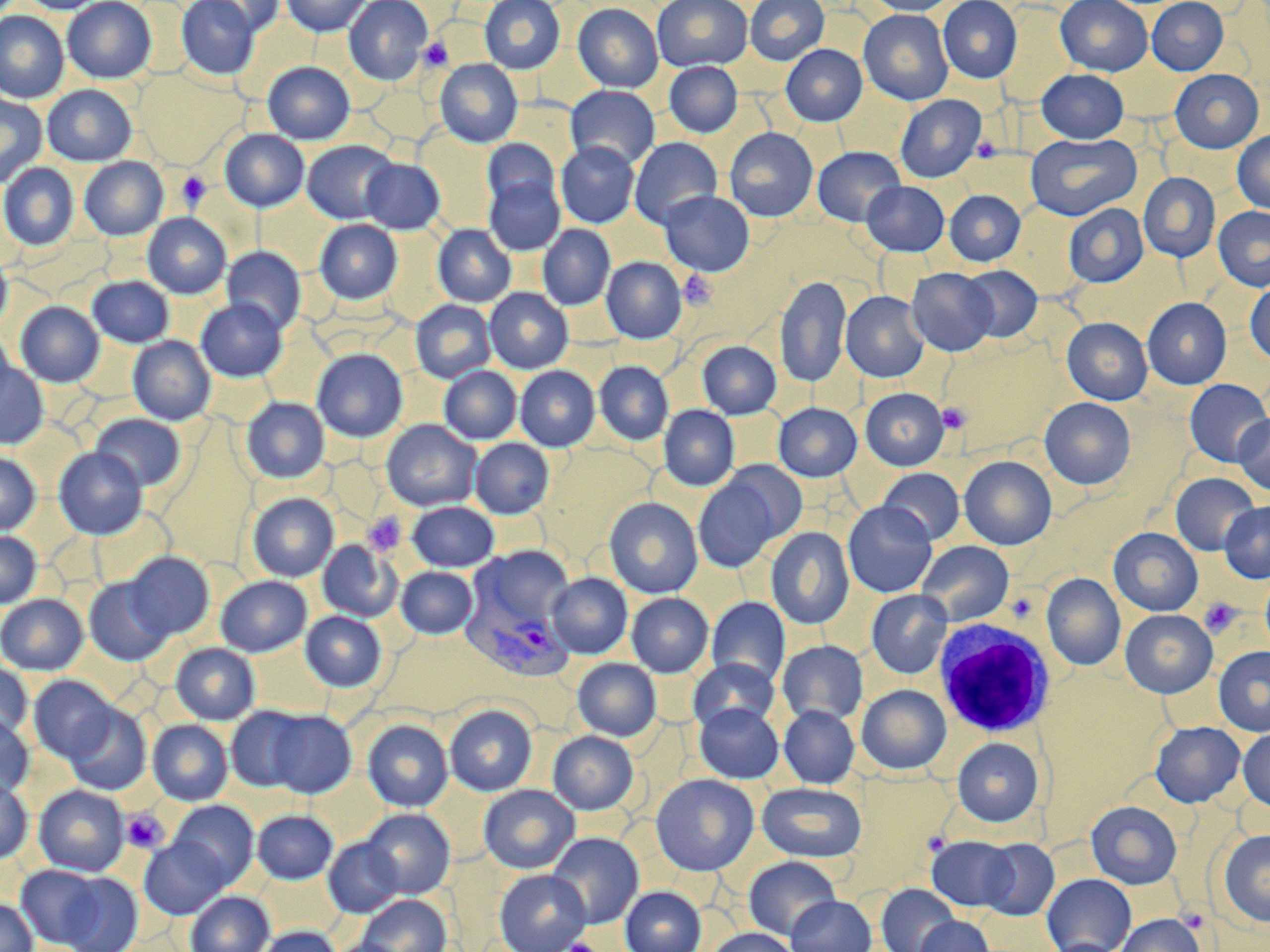

Approximate bounding boxes as [x1, y1, x2, y2] in pixels. Plasmodium vivax-infected red blood cell locations: [462, 591, 574, 681]. White blood cell locations: [932, 617, 1057, 737]. Uninfected red blood cell locations: [19, 0, 106, 14], [62, 0, 156, 83], [176, 0, 260, 80], [200, 0, 283, 36], [281, 0, 369, 36], [344, 0, 432, 85], [480, 0, 565, 74], [652, 0, 753, 72], [745, 0, 829, 65], [865, 0, 959, 15], [1055, 0, 1153, 75], [1147, 0, 1228, 75], [938, 1, 1022, 83], [572, 3, 663, 92], [859, 9, 953, 105], [0, 11, 68, 103], [781, 44, 867, 126], [435, 59, 522, 147], [262, 61, 354, 144], [664, 62, 743, 137], [133, 69, 244, 168], [1036, 69, 1129, 143], [1170, 69, 1264, 153], [42, 85, 137, 166], [565, 85, 660, 169], [0, 92, 47, 189], [895, 94, 986, 183], [724, 127, 818, 221], [219, 129, 309, 212], [1233, 130, 1270, 213], [1026, 134, 1141, 220], [630, 137, 723, 228], [483, 139, 560, 212], [302, 140, 399, 224], [556, 141, 639, 228], [812, 146, 906, 226], [79, 157, 168, 240], [361, 158, 445, 233], [0, 163, 79, 250], [1138, 173, 1220, 262], [484, 175, 565, 256], [862, 181, 949, 256], [944, 189, 1026, 266], [659, 190, 754, 276], [1063, 204, 1148, 287], [1214, 206, 1270, 291], [143, 213, 231, 298], [315, 220, 402, 304], [432, 224, 516, 307], [538, 224, 615, 310], [222, 246, 306, 334], [0, 248, 12, 332], [602, 257, 686, 343], [960, 265, 1043, 342], [907, 267, 998, 356], [775, 275, 851, 388], [88, 276, 174, 347], [1245, 280, 1270, 364], [485, 288, 573, 373], [841, 291, 928, 382], [1142, 297, 1231, 389], [196, 299, 287, 382], [411, 300, 496, 383], [15, 301, 104, 387], [1062, 317, 1152, 404], [0, 330, 15, 411], [128, 336, 215, 425], [697, 340, 781, 419], [312, 349, 408, 441], [0, 360, 48, 448], [594, 361, 673, 444], [515, 365, 599, 451], [439, 366, 521, 444], [1184, 379, 1269, 467], [860, 388, 949, 470], [241, 397, 329, 483], [1040, 397, 1135, 489], [773, 402, 862, 481], [659, 406, 739, 490], [92, 413, 185, 491], [1234, 415, 1270, 495], [381, 420, 481, 511], [470, 438, 554, 518], [54, 447, 147, 539], [0, 451, 40, 534], [960, 456, 1057, 549], [721, 460, 809, 543], [878, 468, 965, 544], [1171, 473, 1260, 555], [694, 476, 783, 572], [247, 492, 338, 581], [604, 497, 702, 598], [408, 501, 499, 571], [843, 501, 937, 597], [1219, 501, 1270, 583], [766, 527, 854, 629], [1108, 528, 1203, 616], [0, 530, 41, 608], [318, 540, 401, 621], [916, 540, 1014, 625], [474, 547, 575, 631], [125, 552, 215, 639], [396, 566, 478, 638], [1261, 572, 1270, 659], [547, 573, 632, 658], [1042, 574, 1125, 670], [216, 575, 312, 656], [84, 578, 171, 666], [866, 589, 953, 678], [627, 593, 713, 677], [0, 594, 88, 674], [706, 597, 791, 686], [1120, 609, 1217, 698], [301, 611, 386, 691], [777, 640, 868, 726], [171, 643, 259, 724], [1214, 647, 1270, 736], [689, 658, 779, 732], [573, 659, 661, 740], [0, 662, 32, 739], [29, 676, 118, 763], [857, 684, 951, 774], [695, 703, 784, 783], [65, 704, 151, 795], [445, 705, 536, 795], [779, 705, 859, 788], [226, 707, 308, 791], [267, 710, 356, 797], [0, 715, 33, 797], [148, 720, 232, 804], [362, 720, 453, 811], [1150, 721, 1245, 807], [1238, 728, 1270, 811], [548, 730, 638, 814], [953, 738, 1043, 826], [651, 774, 758, 875], [0, 777, 32, 863], [757, 782, 866, 862], [479, 784, 579, 873], [34, 785, 129, 875], [169, 800, 258, 888], [1086, 801, 1182, 889], [362, 808, 455, 897], [252, 810, 338, 883], [1218, 830, 1270, 926], [548, 831, 644, 928], [927, 836, 1019, 911], [140, 837, 229, 919], [323, 837, 404, 917], [979, 838, 1059, 920], [743, 856, 841, 940], [16, 865, 107, 948], [495, 869, 591, 952], [58, 872, 143, 952], [1042, 873, 1137, 952], [877, 884, 961, 952], [621, 886, 706, 952], [185, 890, 274, 952], [357, 894, 451, 951], [786, 896, 876, 952], [0, 898, 38, 952], [1117, 914, 1205, 952], [915, 916, 995, 952], [254, 926, 341, 952], [705, 928, 799, 952], [326, 938, 410, 952], [1042, 938, 1126, 952]. Platelet locations: [418, 37, 453, 71], [972, 137, 1003, 163], [176, 171, 212, 210], [680, 270, 716, 309], [937, 402, 971, 433], [362, 512, 407, 555], [1200, 598, 1242, 637], [120, 808, 169, 853], [1179, 907, 1209, 932], [564, 938, 597, 952]. Slide-level diagnosis: Plasmodium vivax. Light microscopy. Captured at 1000x magnification. Thin blood film. Single field of view. May-Grünwald-Giemsa stain. Image is 1270×952 pixels.